Assess the morphology of the red blood cells.
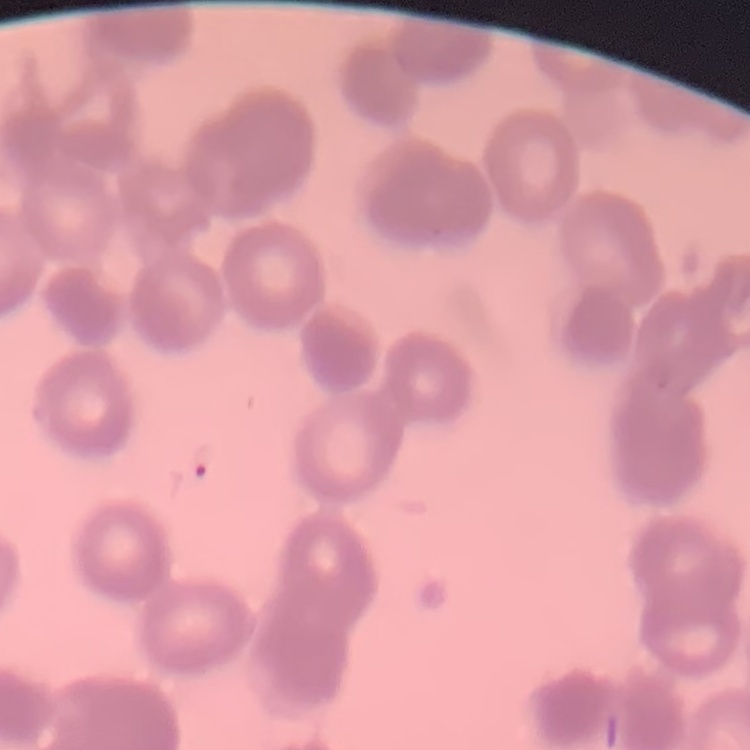
Rouleaux formation.

Stained with either Field's or Giemsa. Thin blood film. One tile cut from a larger photomicrograph.